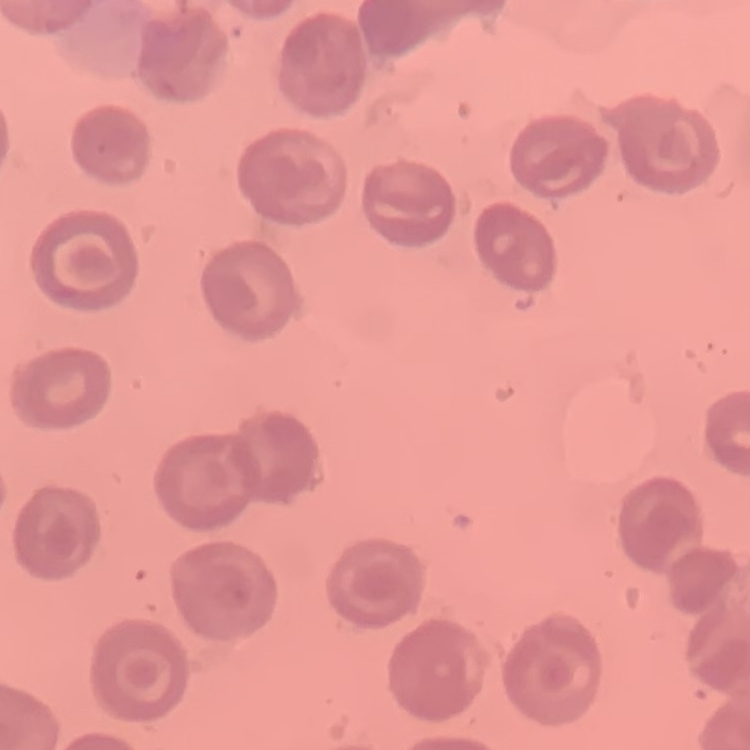

The red blood cells show no rouleaux formation. Field's or Giemsa stain. Thin blood film. Square crop of a larger photomicrograph.